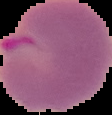 From a thin blood smear. Image is 112×115 pixels. The area outside the segmented cell region is set to black. Malaria status: parasitized.